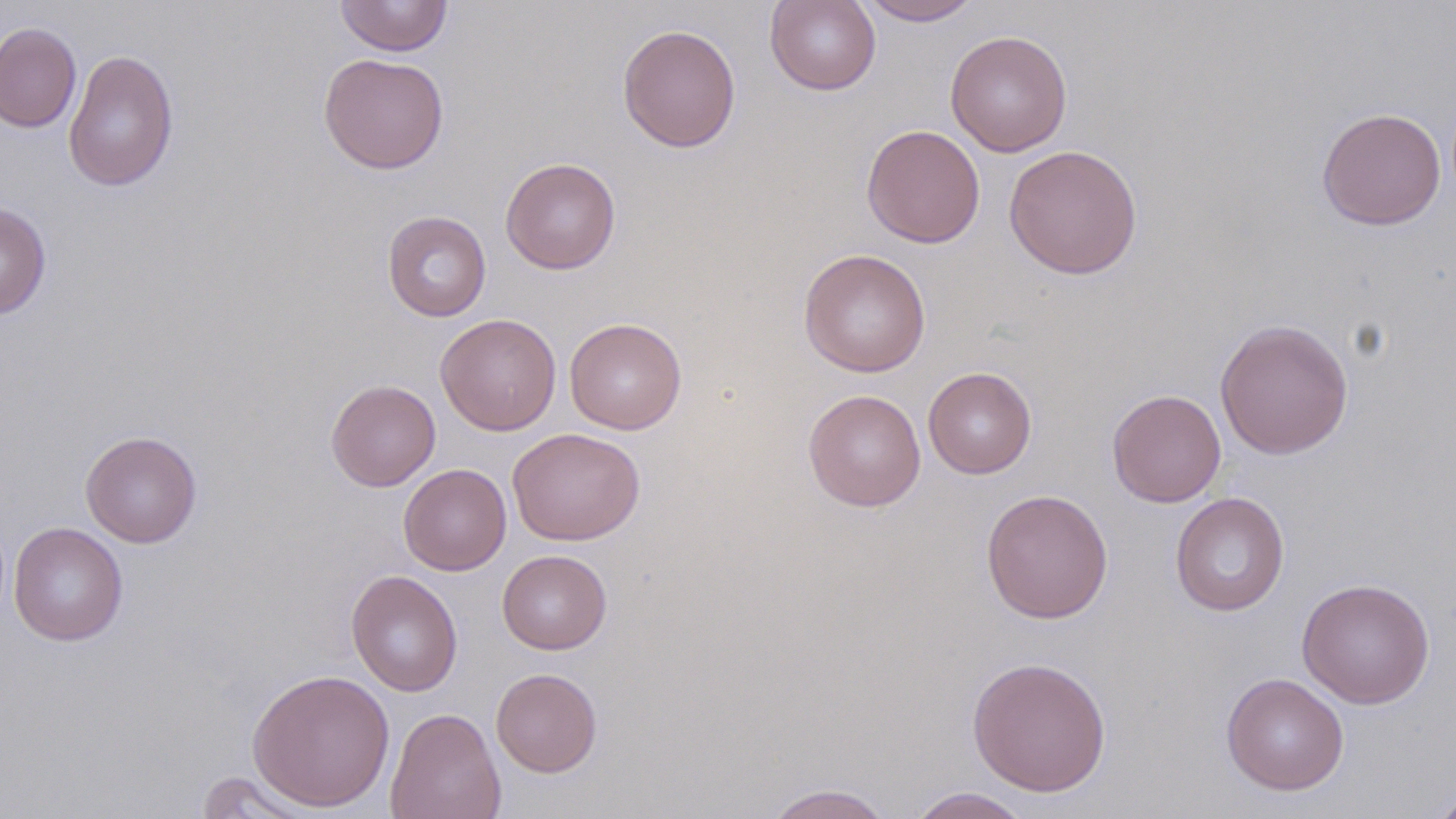
Approximate bounding boxes as [x1, y1, x2, y2] in pixels. Uninfected red blood cell locations: [335, 0, 453, 57], [765, 0, 881, 95], [858, 0, 982, 25], [0, 21, 82, 133], [617, 23, 742, 153], [945, 30, 1072, 157], [63, 48, 179, 193], [318, 52, 449, 174], [1316, 107, 1446, 231], [861, 124, 986, 248], [1003, 144, 1143, 280], [500, 157, 621, 275], [0, 201, 51, 319], [381, 211, 492, 321], [798, 248, 931, 377], [435, 313, 562, 435], [564, 317, 687, 434], [1214, 317, 1354, 460], [923, 367, 1037, 479], [325, 379, 441, 491], [803, 388, 926, 512], [1107, 389, 1226, 507], [507, 427, 645, 546], [80, 430, 202, 548], [398, 463, 511, 575], [980, 488, 1113, 624], [1170, 492, 1290, 616], [8, 523, 128, 645], [497, 550, 612, 654], [346, 570, 463, 697], [1297, 577, 1435, 709], [967, 655, 1112, 797], [247, 668, 395, 811], [490, 668, 603, 777], [1221, 672, 1349, 796], [385, 707, 506, 819], [193, 770, 319, 818], [762, 783, 895, 819], [1428, 786, 1456, 819], [906, 788, 1032, 819]. Slide-level diagnosis: negative for blood parasites. Image is 1456×819 pixels. One field of a larger specimen. Light microscopy. May-Grünwald-Giemsa-stained preparation. 1000x magnification. Thin blood film.